Classify this cell by malaria status.
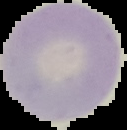
Uninfected.

Summary:
  - Preparation: thin blood film
  - Image size: 127×130 pixels
  - Image type: segmented cell region on a black background